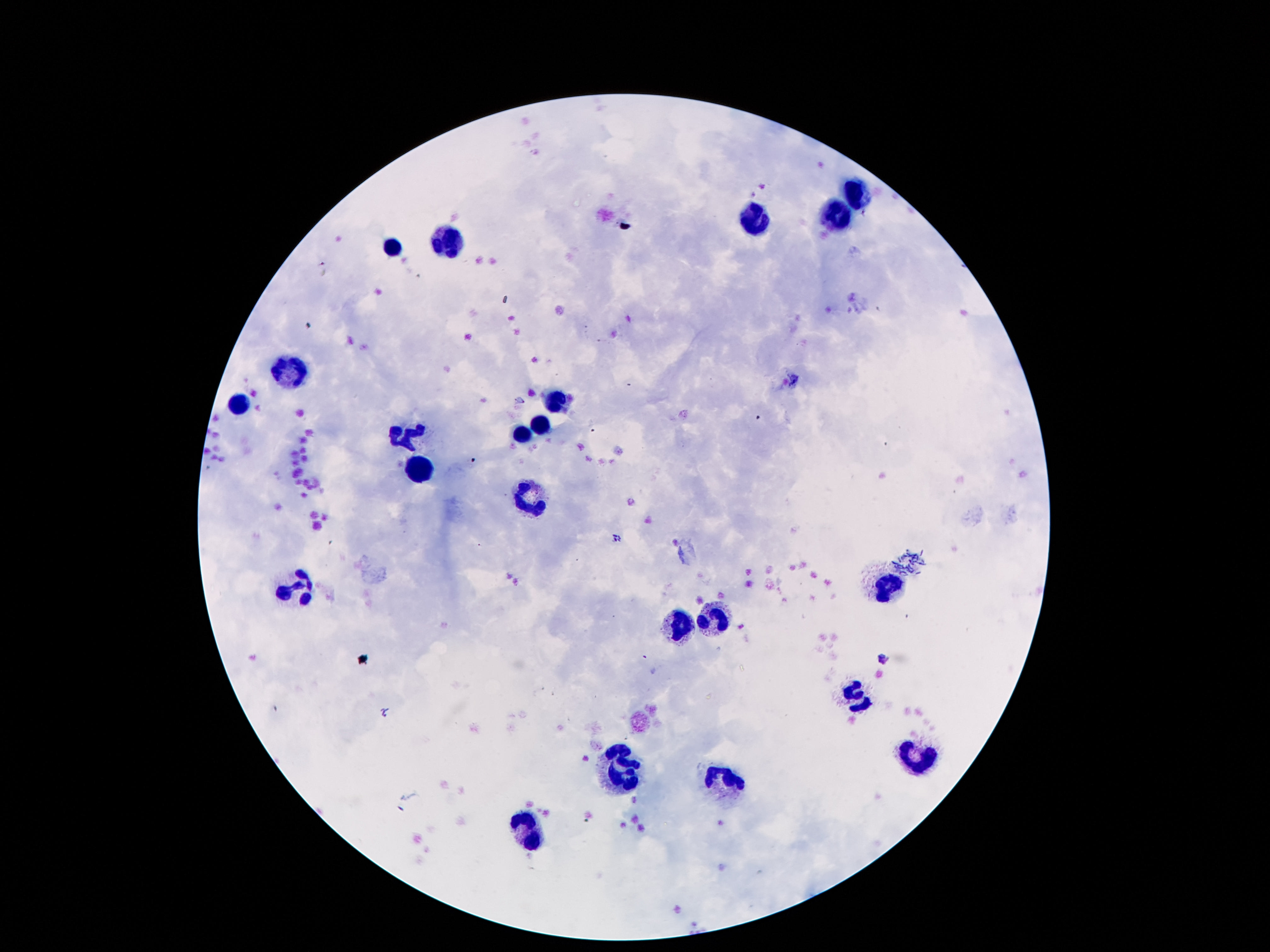
Approximate centers as (x, y) in pixels.
Summary:
  - Leukocyte locations: (859, 194), (836, 215), (754, 218), (451, 240), (393, 246), (290, 367), (241, 399), (561, 404), (542, 423), (523, 434), (402, 438), (425, 472), (530, 490), (299, 586), (885, 588), (717, 618), (675, 623), (862, 697), (920, 760), (626, 769), (731, 781), (528, 832)
  - Field of view: one from this slide
  - Preparation: thick peripheral-blood smear
  - Magnification: 100x
  - Capture: smartphone camera through the microscope eyepiece
  - Stain: Giemsa
  - Image size: 1270×952 pixels
  - Patient malaria status: not infected